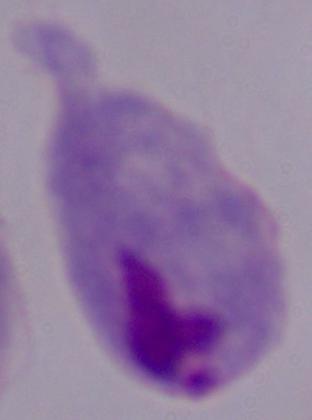

Summary:
  - Magnification: 1000x
  - Modality: micrograph
  - Identification: trichomonad